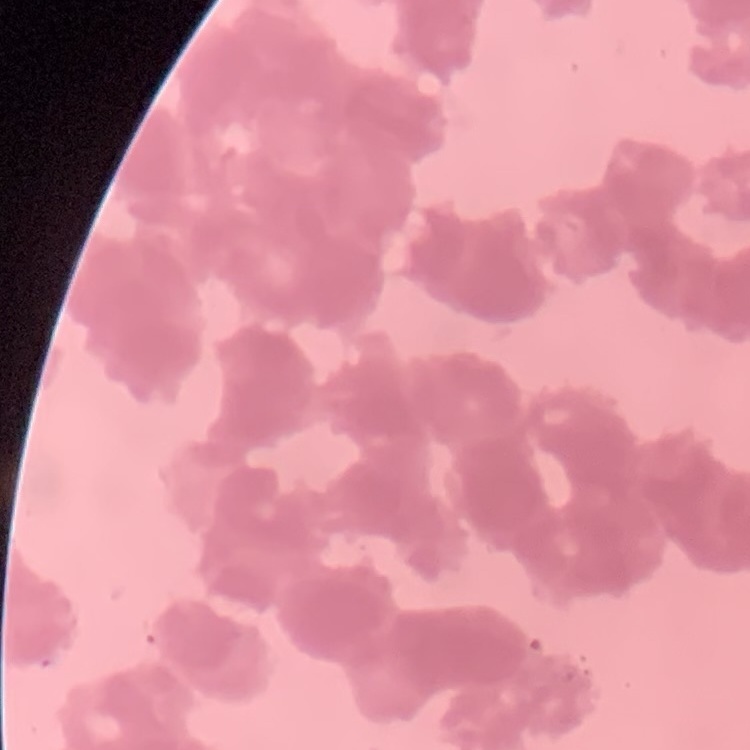

The red blood cells show rouleaux formation. Field's or Giemsa stain. One tile cut from a larger photomicrograph. Thin blood smear.